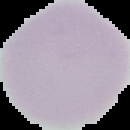
{
  "preparation": "thin blood smear",
  "image_type": "cell region segmented out of the field of view; surrounding area masked to black",
  "malaria_status": "uninfected",
  "image_size": "130×130 pixels"
}